Assess this cell for malaria.
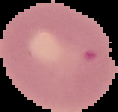
Uninfected.

Image is 118×112 pixels. Cell region segmented out of the field of view; the surrounding area is masked to black. From a thin blood smear.